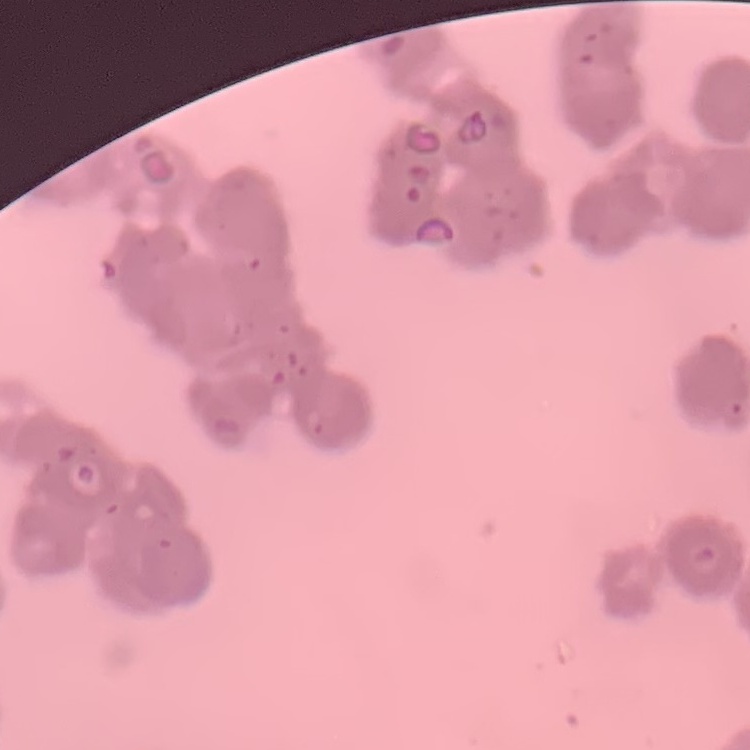

erythrocyte_morphology: rouleaux formation
preparation: thin peripheral smear
image_type: one tile cut from a larger photomicrograph
stain: Field's or Giemsa